Give the extent of all uninfected red blood cells.
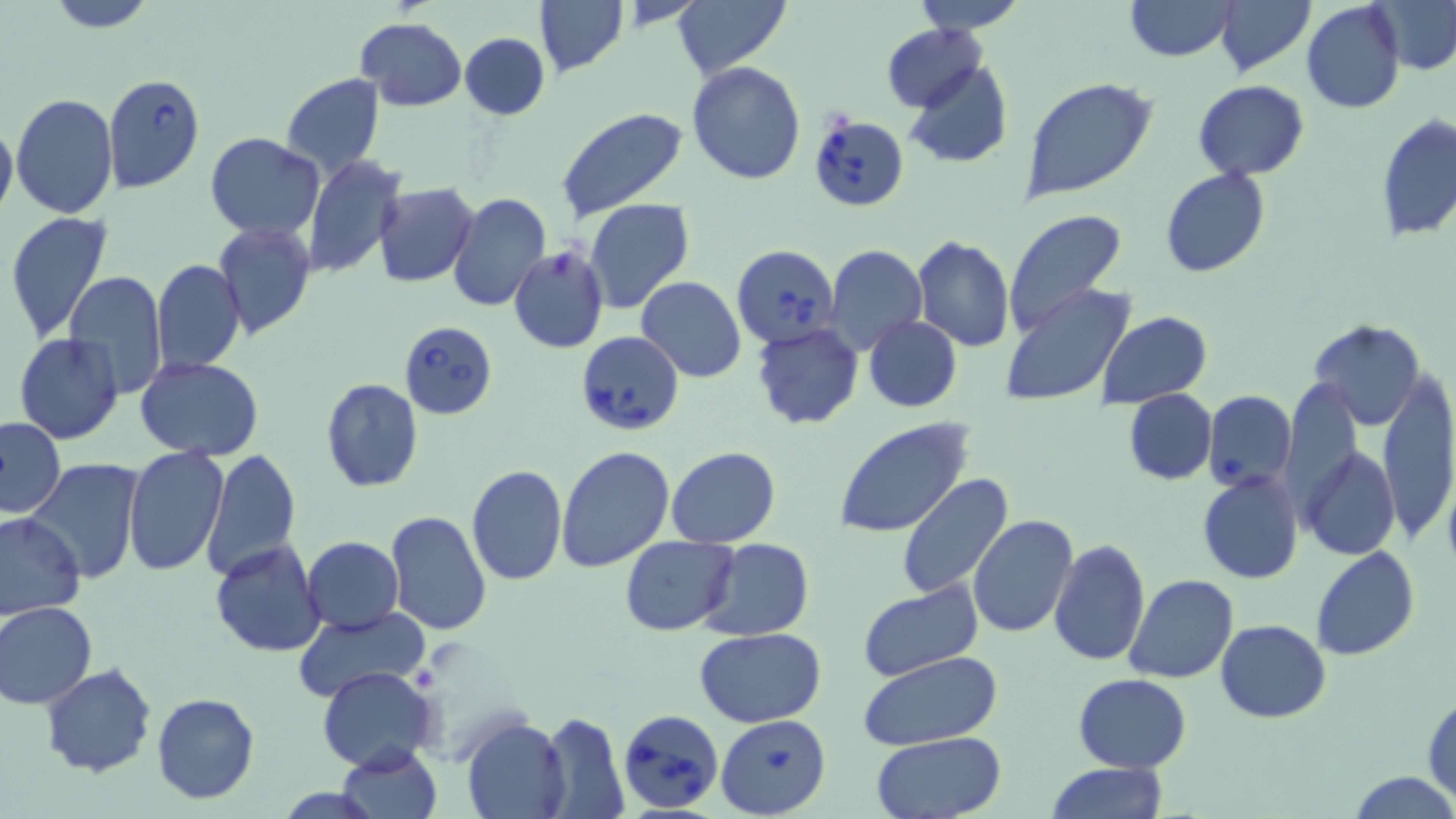
Approximate bounding boxes as (x1,y1)-(x2,y2) corner pairs in pixels.
Uninfected red blood cells: (43,0)-(159,32), (534,0)-(627,79), (671,0)-(792,80), (908,0)-(1029,34), (1125,0)-(1237,61), (1214,0)-(1316,77), (1376,1)-(1456,74), (1302,2)-(1404,114), (355,17)-(467,111), (882,24)-(987,111), (460,33)-(550,120), (686,61)-(808,184), (901,61)-(1013,169), (282,72)-(386,179), (1021,79)-(1157,203), (1193,82)-(1310,179), (10,94)-(119,220), (553,105)-(691,223), (1377,114)-(1456,242), (0,120)-(17,224), (204,132)-(325,239), (301,155)-(405,277), (1160,167)-(1270,278), (372,184)-(479,285), (447,193)-(551,312), (584,199)-(696,315), (1002,209)-(1128,334), (4,211)-(113,342), (212,221)-(315,339), (911,236)-(1015,352), (825,245)-(927,354), (508,246)-(610,354), (152,258)-(246,375), (63,270)-(168,398), (635,276)-(748,382), (998,284)-(1138,408), (1100,312)-(1212,407), (862,315)-(963,413), (1307,319)-(1426,427), (752,322)-(863,429), (13,333)-(124,444), (138,357)-(262,460), (1378,372)-(1455,545), (320,378)-(424,492), (1123,388)-(1216,485), (0,417)-(65,518), (833,418)-(976,539), (1302,444)-(1399,560), (122,445)-(228,576), (555,446)-(674,574), (201,447)-(299,581), (667,447)-(781,547), (24,459)-(148,585), (467,465)-(568,586), (1196,471)-(1304,585), (896,473)-(1017,599), (0,511)-(84,619), (384,511)-(492,635), (968,515)-(1078,638), (620,535)-(737,636), (301,536)-(403,634), (700,538)-(815,639), (1048,538)-(1151,666), (209,540)-(326,657), (1310,547)-(1420,661), (1125,574)-(1240,683), (857,581)-(984,683), (2,600)-(98,709), (291,609)-(426,705), (1215,619)-(1330,722), (695,628)-(825,728), (859,652)-(1002,749), (42,663)-(157,778), (317,665)-(439,771), (1073,674)-(1190,773), (152,692)-(259,804), (1423,692)-(1456,802), (538,711)-(629,818), (462,717)-(570,818), (871,734)-(1007,819), (336,744)-(441,819), (1044,762)-(1169,819), (1348,771)-(1456,818).

Babesia divergens-infected red blood cell locations: (102,74)-(205,191), (810,113)-(910,211), (733,243)-(840,349), (400,320)-(498,419), (576,329)-(685,436), (1203,392)-(1296,490), (619,710)-(725,813), (715,714)-(830,818). Platelet locations: (548,250)-(579,280). Slide-level diagnosis: Babesia divergens. Light microscopy. 1000x magnification. May-Grünwald-Giemsa-stained preparation. One field of a larger specimen. Thin blood smear. Image is 1456×819 pixels.